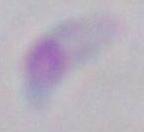
Summary:
  - Magnification: 1000x
  - Modality: micrograph
  - Identification: Toxoplasma gondii